Evaluate for malaria.
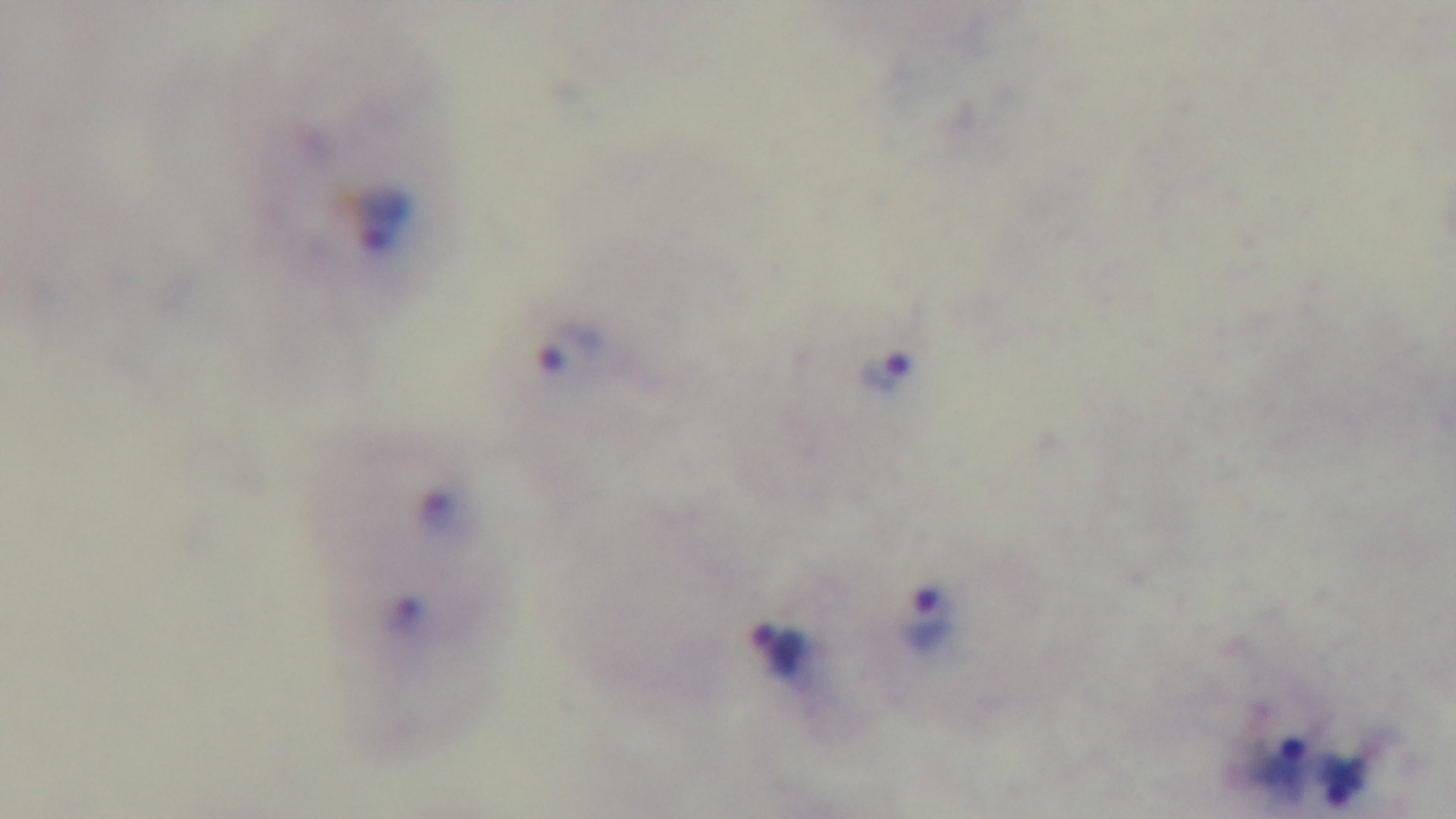
It is infected.

{
  "preparation": "thick blood film",
  "capture": "mounted 4K digital camera",
  "stain": "Giemsa",
  "modality": "light microscopy",
  "objective": "100x oil immersion",
  "field_of_view": "single"
}